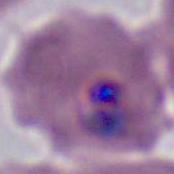
Summary:
  - Identification: Plasmodium
  - Modality: micrograph
  - Magnification: 400x or 1000x